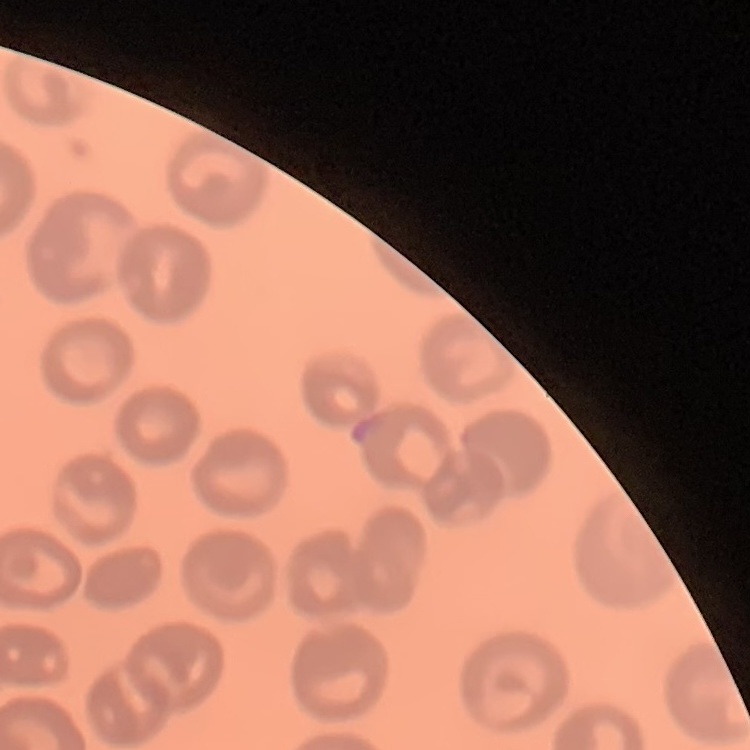

erythrocyte_morphology: no rouleaux formation
stain: Field's or Giemsa
image_type: one tile cut from a larger photomicrograph
preparation: thin peripheral smear